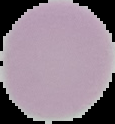 Image is 115×124 pixels. Result: no malaria parasites detected. Cell region segmented out of the field of view; the surrounding area is masked to black. From a thin blood film.